Identify the cell.
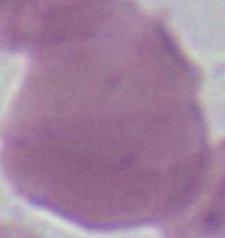
An erythrocyte.

modality = micrograph
magnification = 1000x